Evaluate for Plasmodium parasites.
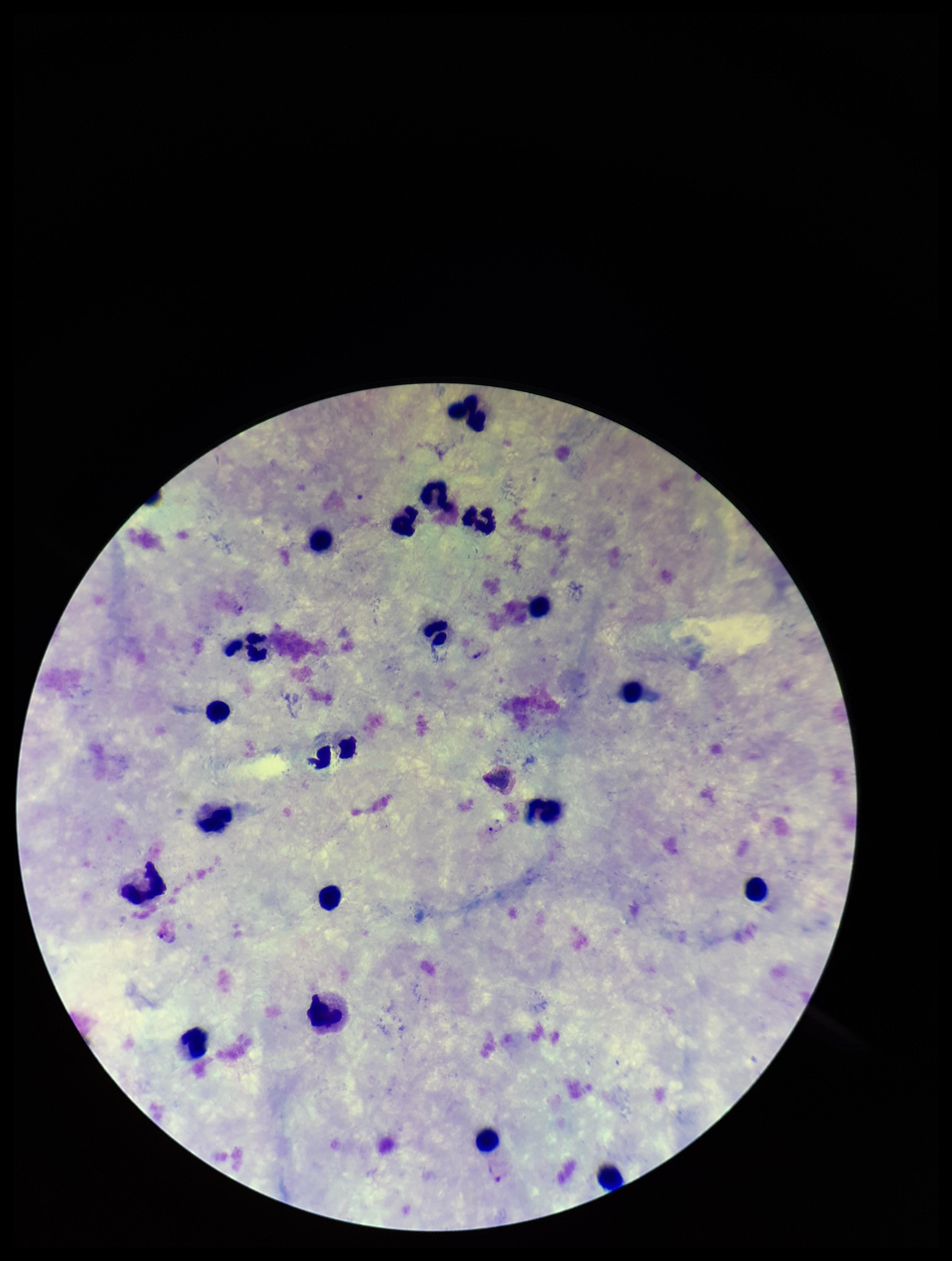
Detected.

Summary:
  - Image size: 952×1261 pixels
  - Patient malaria status: positive
  - Leukocyte count: 22
  - Species reported for this patient: Plasmodium vivax
  - Stain: Giemsa
  - Parasite count: 2
  - Field of view: one from this slide
  - Preparation: thick blood smear
  - Capture: smartphone photograph through the microscope eyepiece